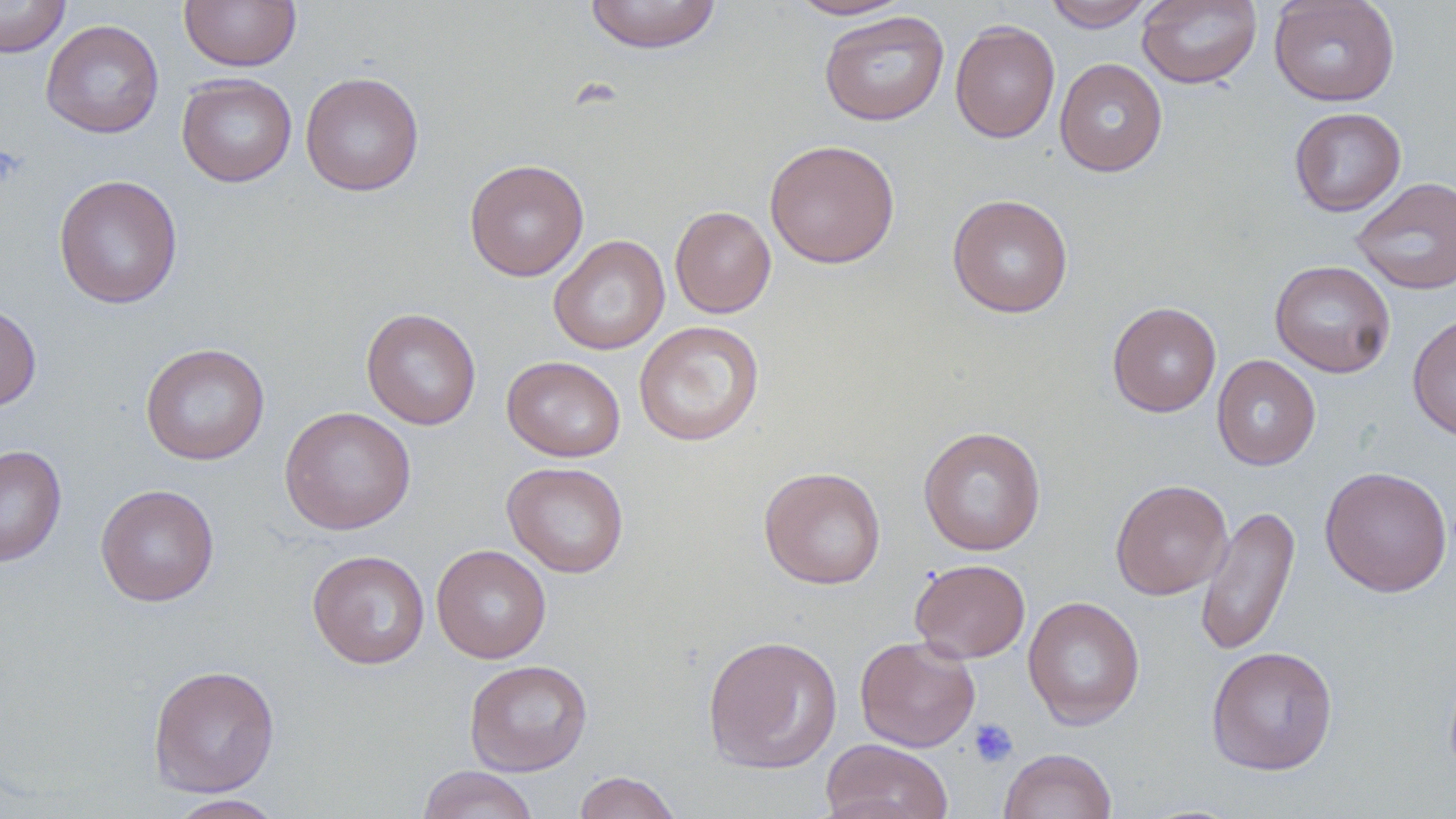
Approximate bounding boxes as [x1, y1, x2, y2] in pixels. Platelet locations: [968, 718, 1018, 768]. Uninfected red blood cell locations: [0, 0, 70, 58], [179, 0, 302, 71], [584, 0, 723, 54], [785, 0, 913, 20], [1041, 0, 1153, 31], [1137, 0, 1262, 89], [1269, 0, 1401, 106], [819, 10, 949, 126], [41, 20, 164, 138], [950, 20, 1060, 143], [1055, 59, 1168, 177], [300, 72, 424, 196], [176, 73, 297, 187], [1289, 107, 1406, 216], [764, 139, 901, 268], [464, 159, 589, 281], [53, 174, 183, 309], [1351, 176, 1455, 295], [946, 194, 1074, 318], [670, 206, 776, 318], [549, 234, 670, 355], [1269, 259, 1396, 378], [1107, 301, 1222, 417], [0, 302, 41, 412], [361, 308, 482, 430], [1407, 311, 1456, 442], [633, 320, 765, 446], [140, 342, 270, 465], [1211, 354, 1321, 471], [502, 355, 626, 462], [279, 406, 416, 535], [918, 426, 1047, 556], [0, 444, 67, 567], [502, 461, 630, 577], [1319, 465, 1452, 598], [758, 467, 887, 589], [1110, 479, 1233, 600], [95, 484, 220, 606], [1196, 504, 1300, 658], [431, 544, 551, 663], [306, 550, 430, 669], [909, 558, 1031, 663], [1022, 595, 1145, 730], [702, 634, 843, 774], [855, 635, 980, 752], [1205, 645, 1339, 776], [464, 659, 592, 777], [148, 664, 280, 797], [821, 738, 954, 819], [998, 748, 1118, 819], [416, 765, 540, 819], [574, 771, 683, 819], [165, 794, 287, 818]. Slide-level diagnosis: no evidence of blood parasites. May-Grünwald-Giemsa stain. Thin blood smear. Image is 1456×819 pixels. Captured at 1000x magnification. Single field of view. Light microscopy.